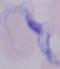

Summary:
  - Magnification: 1000x
  - Modality: photomicrograph
  - Identification: trypanosome